Classify this cell by malaria status.
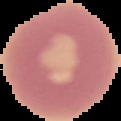

It is uninfected.

Cell region segmented out of the field of view; the surrounding area is masked to black. From a thin blood smear. Image is 121×121 pixels.